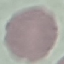

result = negative for malaria parasites
capture = smartphone through the microscope eyepiece
image type = automatically extracted cell patch, resized to 64 × 64 pixels
preparation = thin blood smear
stain = Giemsa